Identify the cell.
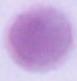
An erythrocyte.

Photomicrograph. 1000x magnification.